Report the malaria status of this cell.
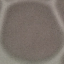
It is uninfected.

Giemsa stain. Thin blood smear. Automatically extracted cell patch, resized to 64 × 64 pixels. Acquired by smartphone through the microscope eyepiece.